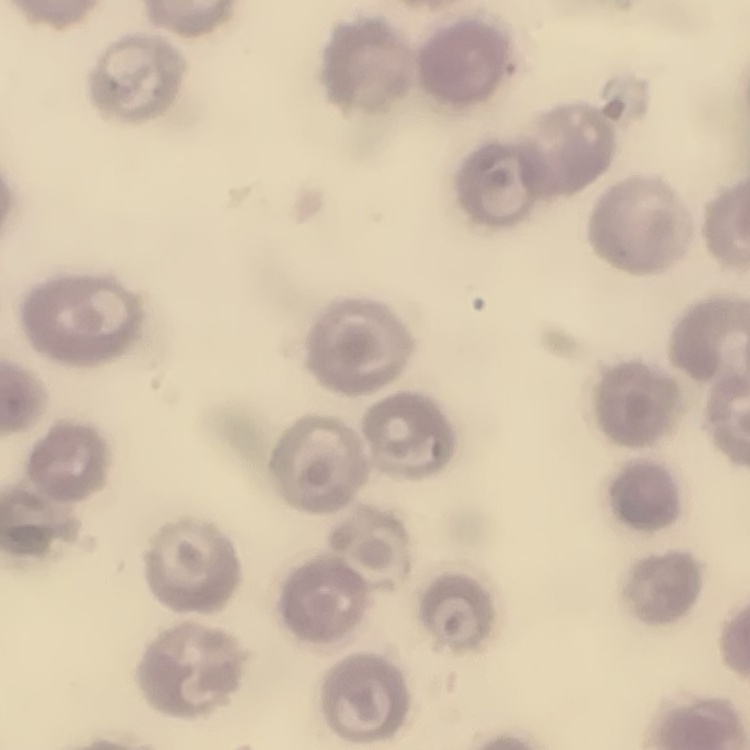
The erythrocytes exhibit no rouleaux formation. Thin peripheral smear. Stained with either Field's or Giemsa. One tile cut from a larger photomicrograph.